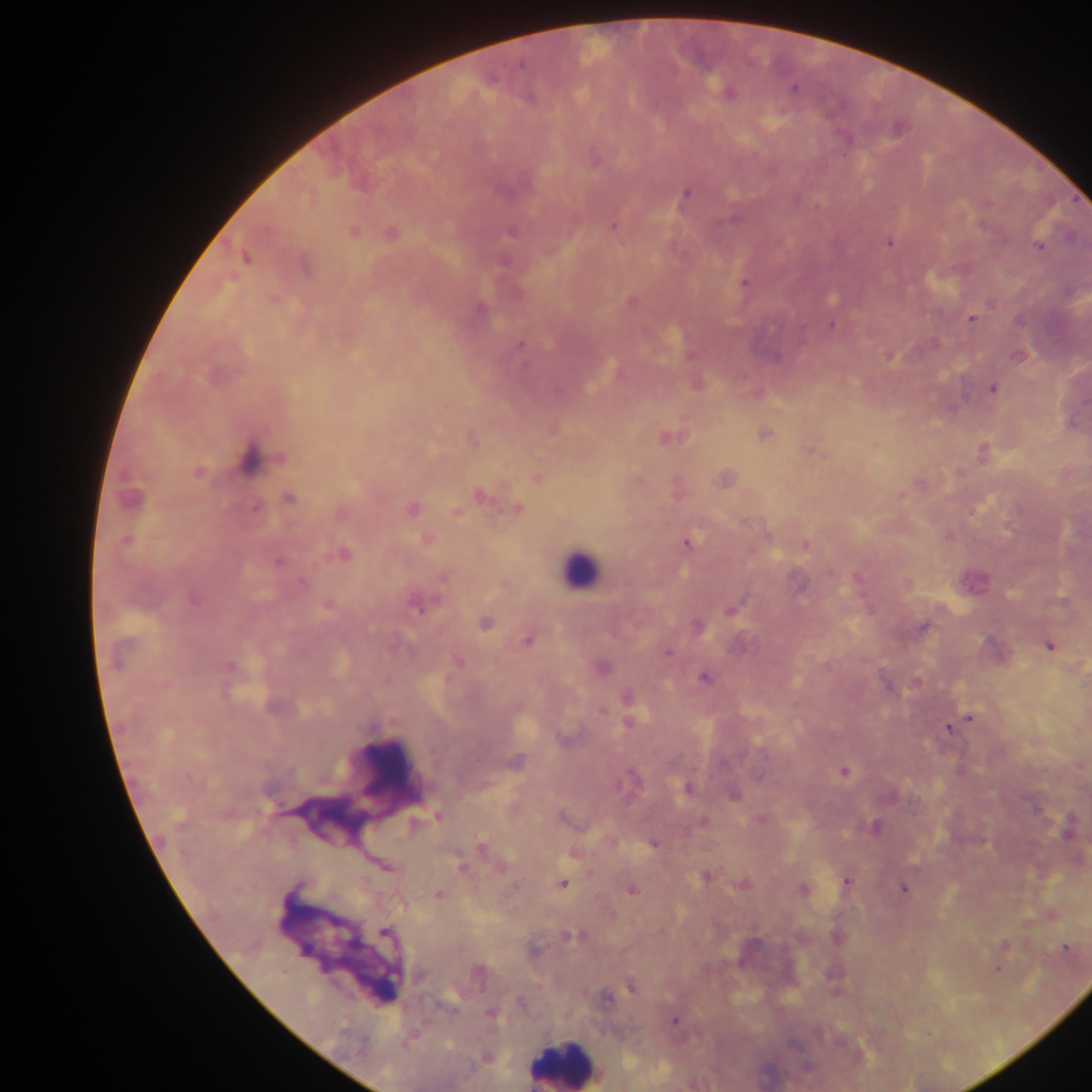
Approximate centers as x y in pixels.
Summary:
  - Leukocyte locations: 579 571; 382 772; 329 820; 563 1064
  - Plasmodium parasite locations: 521 65; 793 88; 728 93; 685 194; 988 203; 733 219; 613 227; 353 232; 511 232; 391 233; 889 243; 1039 247; 245 258; 743 283; 631 302; 480 308; 972 319; 831 325; 520 346; 689 355; 890 355; 776 356; 1017 356; 993 389; 765 434; 666 438; 473 441; 813 453; 279 458; 248 459; 198 473; 538 478; 479 495; 130 498; 289 498; 256 507; 412 509; 517 509; 457 511; 126 540; 426 540; 687 543; 805 545; 343 554; 278 562; 858 578; 443 579; 302 582; 800 585; 193 600; 328 606; 417 606; 732 609; 485 623; 697 625; 923 627; 527 641; 1049 645; 667 652; 458 662; 230 666; 602 668; 705 678; 916 683; 627 697; 602 711; 970 718; 628 723; 948 728; 561 739; 515 763; 844 771; 632 778; 688 788; 734 795; 438 815; 562 818; 703 821; 875 827; 1068 829; 653 844; 482 845; 573 854; 385 866; 462 867; 706 877; 847 882; 563 884; 743 885; 802 889; 904 889; 631 890; 439 895; 402 905; 385 933; 570 936; 1004 945; 1066 948; 534 950; 998 970; 478 972; 420 977; 632 986; 606 998; 521 1003; 449 1004; 492 1015; 674 1020; 485 1058; 807 1067
  - Capture: mobile-phone photograph through a microscope
  - Field of view: single
  - Preparation: thick blood smear
  - Country: Ghana
  - Image size: 1092×1092 pixels